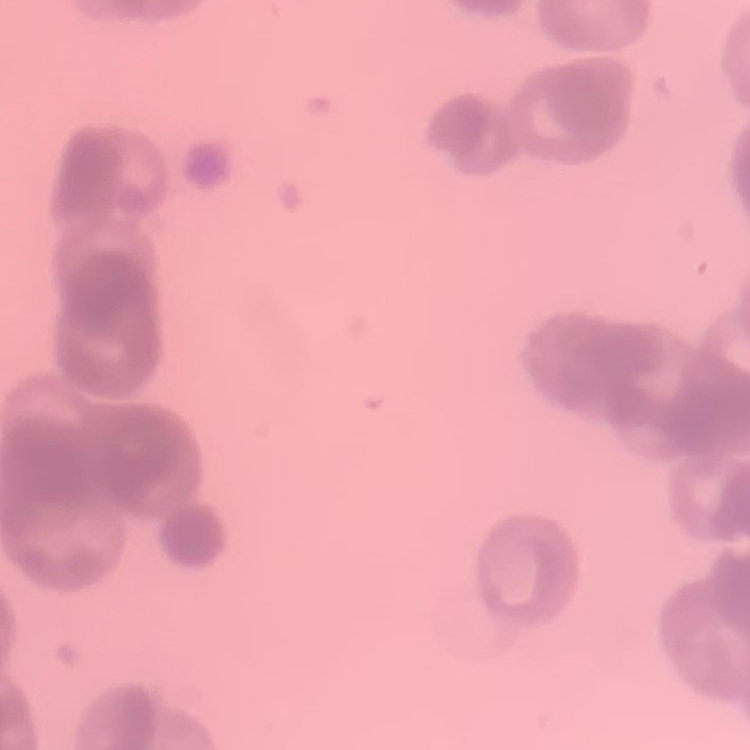

The red blood cells show rouleaux formation. Thin blood smear. One tile cut from a larger photomicrograph. Stained with either Field's or Giemsa.